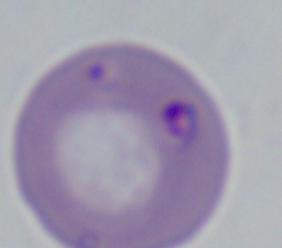
magnification: 1000x
modality: photomicrograph
identification: Babesia